Identify the parasite.
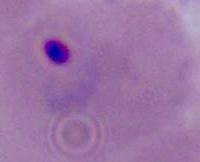
Plasmodium.

Summary:
  - Modality: micrograph
  - Magnification: 400x or 1000x